Comment on the morphology of the red blood cells.
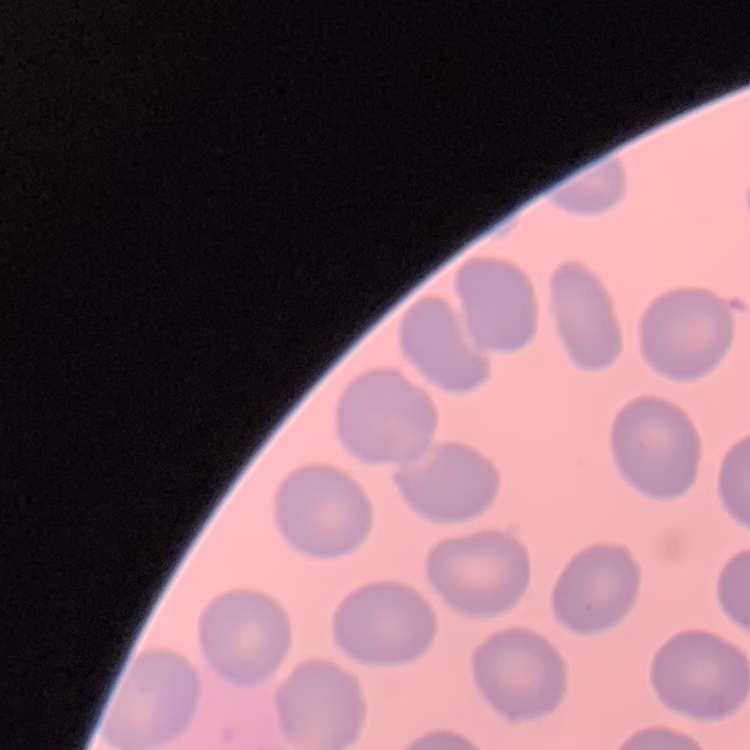

No rouleaux formation.

One tile cut from a larger photomicrograph. Stained with either Field's or Giemsa. Thin blood film.